State the blood parasite species.
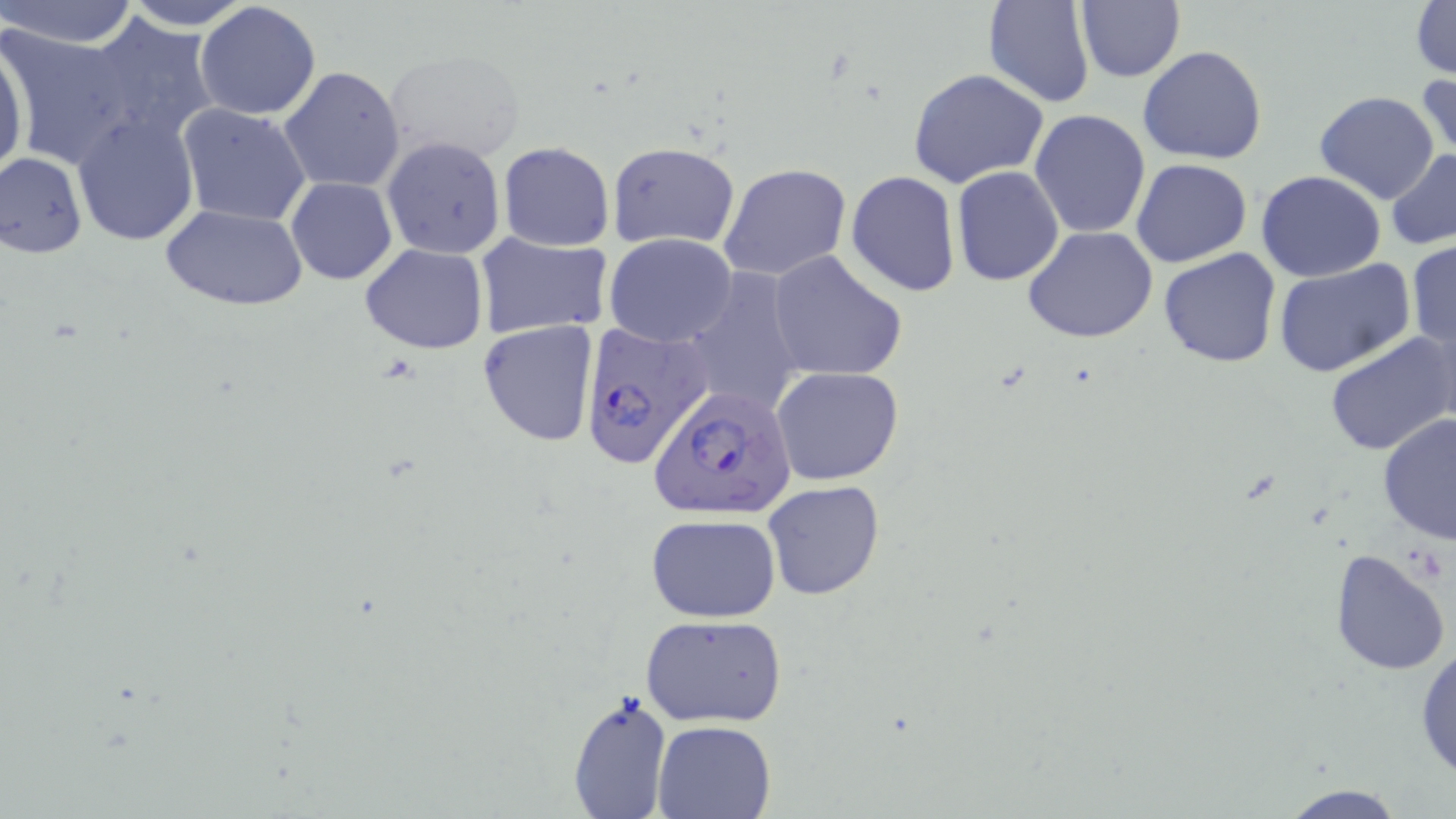
Plasmodium falciparum.

Approximate bounding boxes as named x1/y1/x2/y2 corners in pixels. Uninfected red blood cell locations: (x1=4, y1=0, x2=141, y2=47), (x1=120, y1=0, x2=256, y2=29), (x1=1075, y1=0, x2=1186, y2=83), (x1=1411, y1=0, x2=1456, y2=79), (x1=195, y1=1, x2=321, y2=121), (x1=982, y1=2, x2=1095, y2=108), (x1=84, y1=16, x2=222, y2=149), (x1=1, y1=23, x2=137, y2=167), (x1=0, y1=34, x2=28, y2=186), (x1=1138, y1=45, x2=1269, y2=164), (x1=382, y1=48, x2=526, y2=167), (x1=278, y1=65, x2=405, y2=193), (x1=908, y1=68, x2=1049, y2=188), (x1=1417, y1=71, x2=1456, y2=164), (x1=1313, y1=92, x2=1440, y2=205), (x1=176, y1=103, x2=313, y2=225), (x1=1030, y1=110, x2=1151, y2=239), (x1=71, y1=113, x2=200, y2=247), (x1=380, y1=135, x2=507, y2=260), (x1=496, y1=140, x2=615, y2=252), (x1=606, y1=140, x2=741, y2=249), (x1=1386, y1=148, x2=1456, y2=250), (x1=0, y1=151, x2=88, y2=259), (x1=1132, y1=159, x2=1253, y2=268), (x1=718, y1=163, x2=852, y2=281), (x1=950, y1=166, x2=1065, y2=286), (x1=1256, y1=170, x2=1386, y2=281), (x1=846, y1=171, x2=961, y2=297), (x1=286, y1=176, x2=397, y2=285), (x1=160, y1=203, x2=309, y2=310), (x1=1023, y1=227, x2=1158, y2=344), (x1=472, y1=232, x2=613, y2=341), (x1=604, y1=233, x2=739, y2=348), (x1=1407, y1=239, x2=1456, y2=355), (x1=359, y1=244, x2=488, y2=353), (x1=1158, y1=247, x2=1283, y2=368), (x1=767, y1=250, x2=907, y2=383), (x1=1272, y1=260, x2=1415, y2=378), (x1=680, y1=268, x2=808, y2=418), (x1=478, y1=320, x2=597, y2=448), (x1=1324, y1=331, x2=1456, y2=459), (x1=771, y1=364, x2=905, y2=487), (x1=1377, y1=414, x2=1456, y2=543), (x1=762, y1=481, x2=886, y2=601), (x1=645, y1=514, x2=782, y2=621), (x1=1330, y1=548, x2=1452, y2=677), (x1=640, y1=614, x2=787, y2=727), (x1=1414, y1=644, x2=1456, y2=779), (x1=566, y1=690, x2=675, y2=819), (x1=654, y1=720, x2=776, y2=818), (x1=1271, y1=781, x2=1413, y2=818). Plasmodium falciparum-infected red blood cell locations: (x1=577, y1=320, x2=713, y2=468), (x1=648, y1=387, x2=796, y2=521). Thin blood film. Captured at 1000x magnification. Single field of view. May-Grünwald-Giemsa-stained preparation. Image is 1456×819 pixels. Light microscopy.